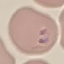
Summary:
  - Malaria status: parasitized
  - Preparation: thin smear
  - Image type: cell patch, automatically extracted from a larger field of view and resized to 64 × 64 pixels
  - Stain: Giemsa
  - Capture: smartphone camera at the microscope eyepiece